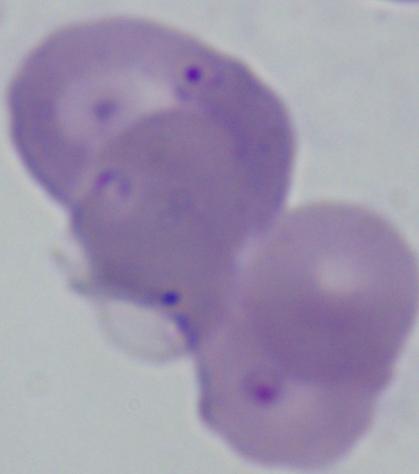

identification = Babesia
modality = photomicrograph
magnification = 1000x